Assess this cell for malaria.
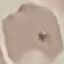

It is uninfected.

Giemsa-stained preparation. Photographed with a smartphone camera at the microscope eyepiece. Thin blood film. Cell patch, automatically extracted from a larger field of view and resized to 64 × 64 pixels.